Classify this cell by malaria status.
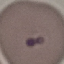

Uninfected.

Giemsa stain. Cell patch, automatically extracted from a larger field of view and resized to 64 × 64 pixels. Thin smear of blood. Acquired by smartphone through the microscope eyepiece.